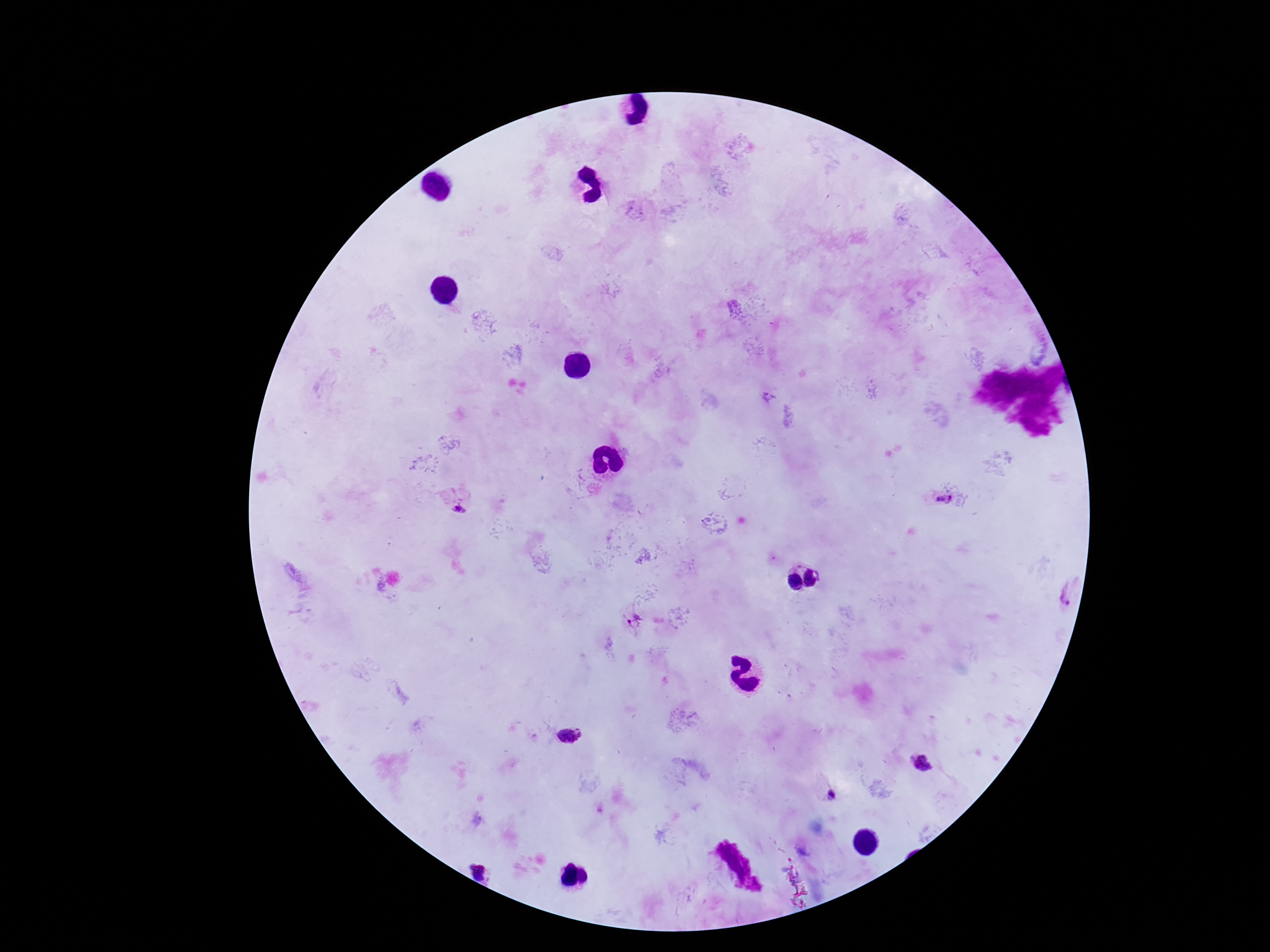
Approximate centers as {x, y} in pixels. Plasmodium parasite locations: {944, 499}, {459, 510}, {817, 577}, {793, 584}, {1059, 591}, {633, 619}, {570, 736}, {926, 765}, {829, 793}, {482, 869}. One field from this slide. 100x magnification. Patient malaria status: infected. Thick peripheral-blood smear. Image is 1270×952 pixels. Giemsa-stained preparation. Photographed through the microscope eyepiece with a smartphone camera.